Identify the cell.
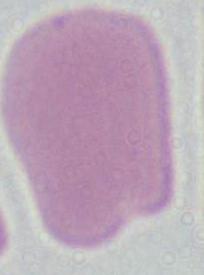

This is an erythrocyte.

modality = micrograph
magnification = 1000x